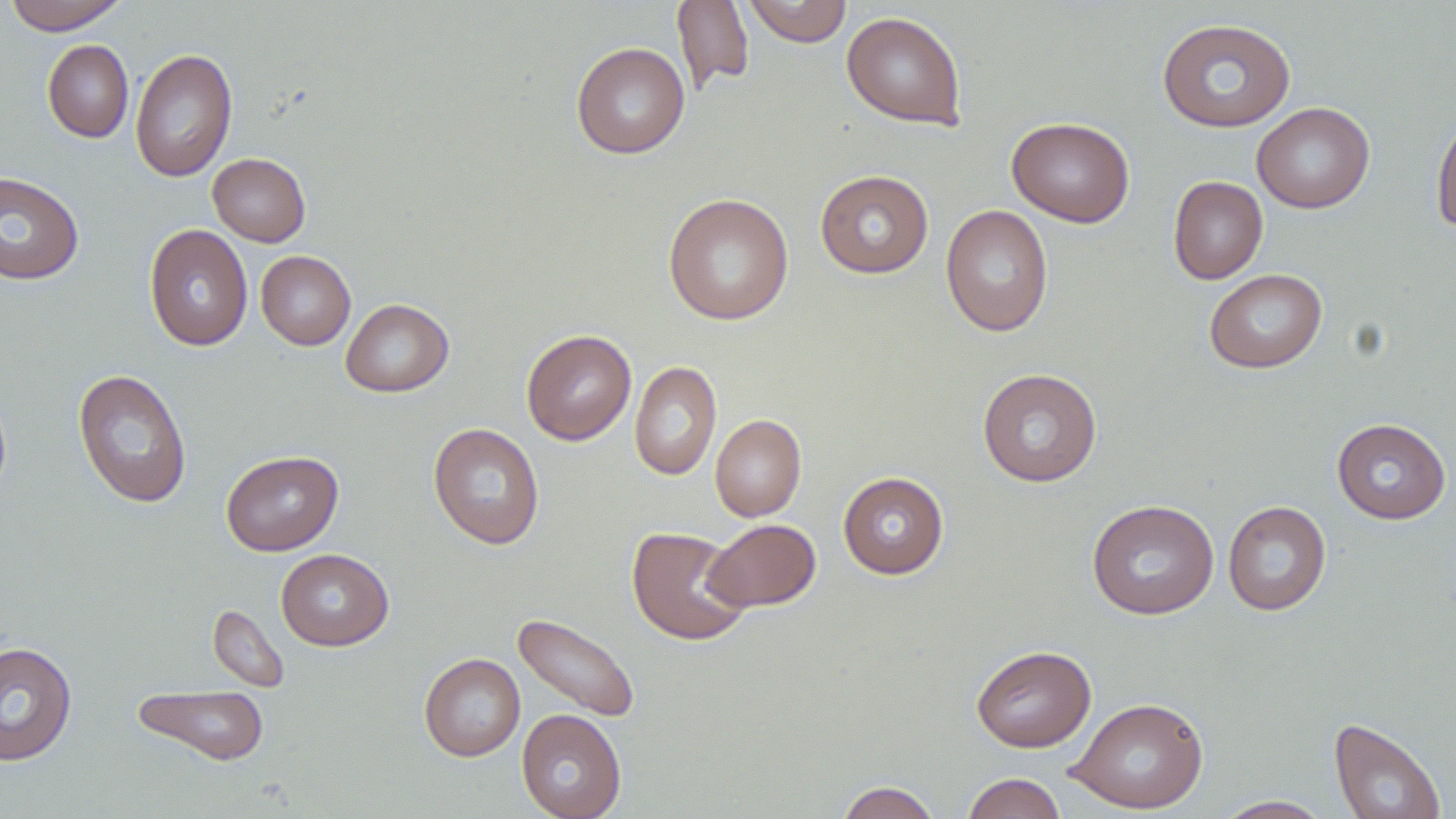

Approximate bounding boxes as [x1, y1, x2, y2] in pixels. Uninfected red blood cell locations: [3, 0, 130, 35], [742, 0, 853, 47], [672, 1, 754, 93], [841, 11, 967, 130], [1157, 18, 1296, 132], [42, 39, 133, 143], [571, 42, 690, 159], [130, 47, 238, 183], [1252, 102, 1374, 213], [1431, 112, 1456, 235], [1006, 116, 1135, 227], [208, 153, 311, 246], [814, 169, 934, 278], [0, 170, 85, 285], [1168, 176, 1268, 284], [663, 193, 794, 325], [940, 205, 1053, 337], [143, 224, 253, 351], [255, 250, 356, 350], [1204, 269, 1328, 373], [340, 298, 453, 397], [521, 329, 636, 445], [629, 360, 722, 480], [977, 368, 1102, 487], [73, 369, 192, 509], [710, 414, 806, 522], [1332, 417, 1450, 524], [427, 422, 545, 550], [221, 450, 344, 556], [838, 471, 949, 579], [1087, 499, 1219, 620], [1222, 500, 1331, 616], [703, 519, 821, 613], [626, 526, 753, 646], [276, 548, 394, 650], [207, 603, 289, 693], [512, 612, 641, 723], [0, 641, 77, 766], [971, 644, 1096, 752], [419, 653, 525, 761], [132, 684, 270, 766], [1067, 696, 1209, 814], [516, 709, 627, 819], [1329, 717, 1447, 819], [962, 772, 1067, 819], [836, 780, 941, 819], [1213, 795, 1333, 818]. Slide-level diagnosis: no evidence of blood parasites. May-Grünwald-Giemsa stain. Single field of view. Image is 1456×819 pixels. Light microscopy. 1000x magnification. Thin blood film.